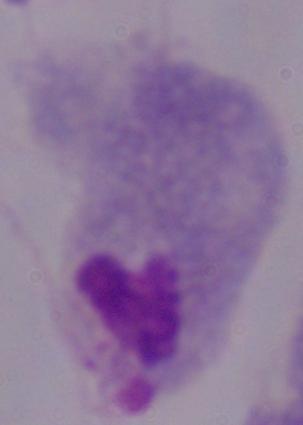

Summary:
  - Modality: photomicrograph
  - Identification: trichomonad
  - Magnification: 1000x